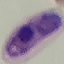

Malaria status: parasitized. Acquired by smartphone through the microscope eyepiece. Automatically extracted cell patch, resized to 64 × 64 pixels. Thin blood smear. Giemsa-stained preparation.